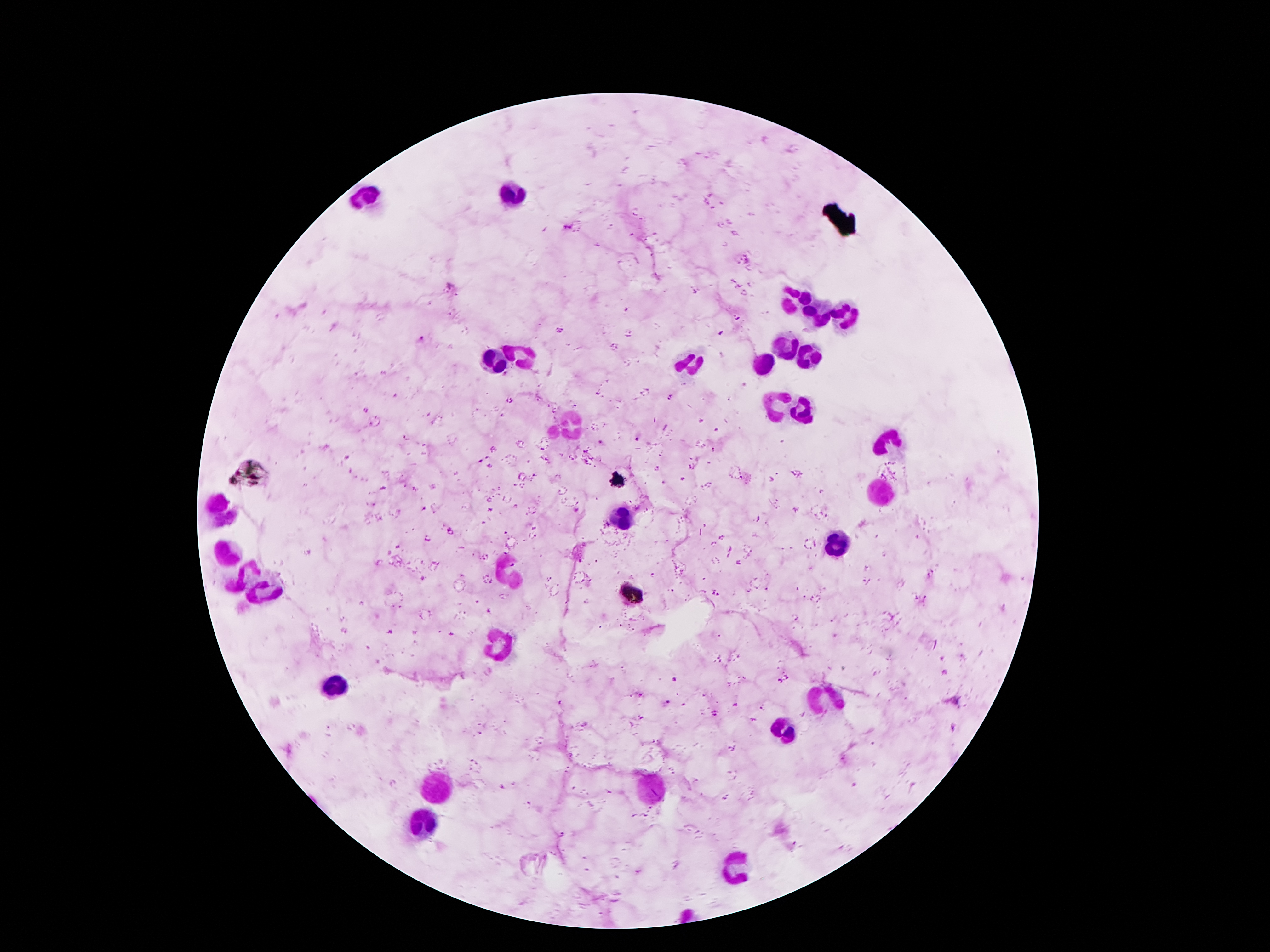
Approximate centers as (x, y) in pixels.
Summary:
  - Malaria parasite locations: (567, 228), (449, 286), (421, 339), (637, 436), (601, 444), (479, 459), (491, 467), (577, 511), (675, 680), (665, 703)
  - Leukocyte locations: (511, 195), (368, 199), (792, 299), (844, 311), (817, 313), (785, 345), (526, 353), (808, 358), (495, 360), (688, 360), (763, 361), (781, 408), (801, 408), (567, 426), (890, 440), (881, 492), (220, 508), (622, 520), (837, 544), (225, 553), (508, 572), (499, 644), (334, 685), (829, 701), (781, 730), (440, 785), (647, 788), (422, 822), (731, 865)
  - Preparation: thick blood smear
  - Magnification: 100x
  - Field of view: single
  - Image size: 1270×952 pixels
  - Stain: Giemsa
  - Patient malaria status: positive for Plasmodium falciparum
  - Capture: smartphone camera through the microscope eyepiece